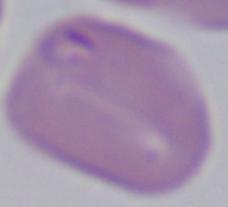

magnification = 1000x
identification = Babesia
modality = micrograph